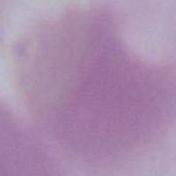

Summary:
  - Identification: erythrocyte
  - Magnification: 1000x
  - Modality: micrograph